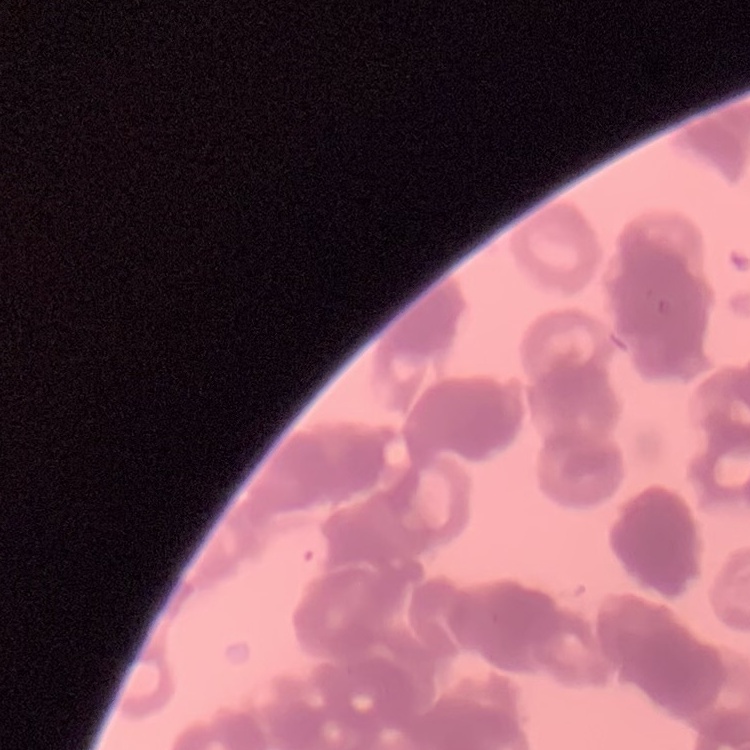 The red blood cells show rouleaux formation. Field's or Giemsa stain. Thin peripheral smear. Square crop of a larger photomicrograph.